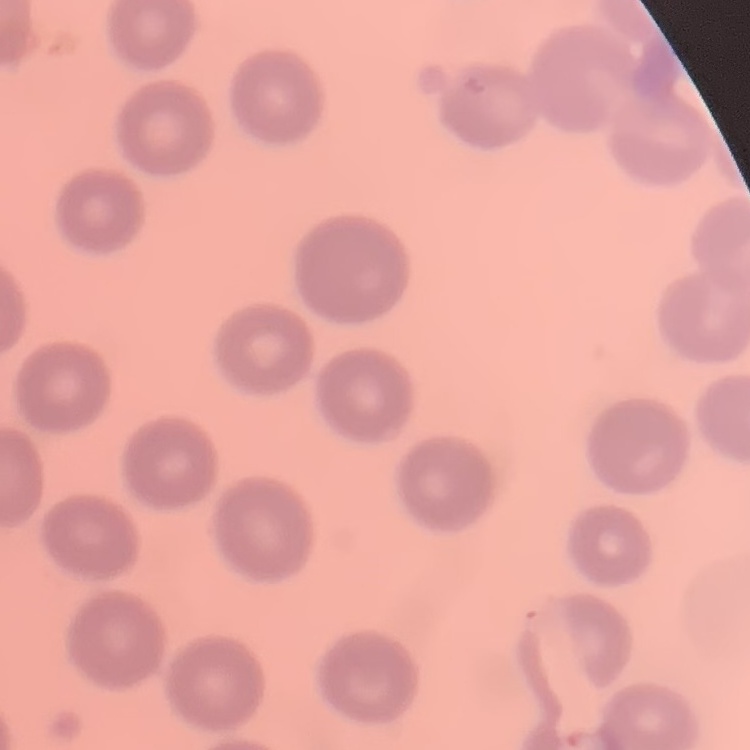

Summary:
  - Erythrocyte morphology: no rouleaux formation
  - Stain: Field's or Giemsa
  - Image type: one tile cut from a larger photomicrograph
  - Preparation: thin blood film